Point out each leukocyte.
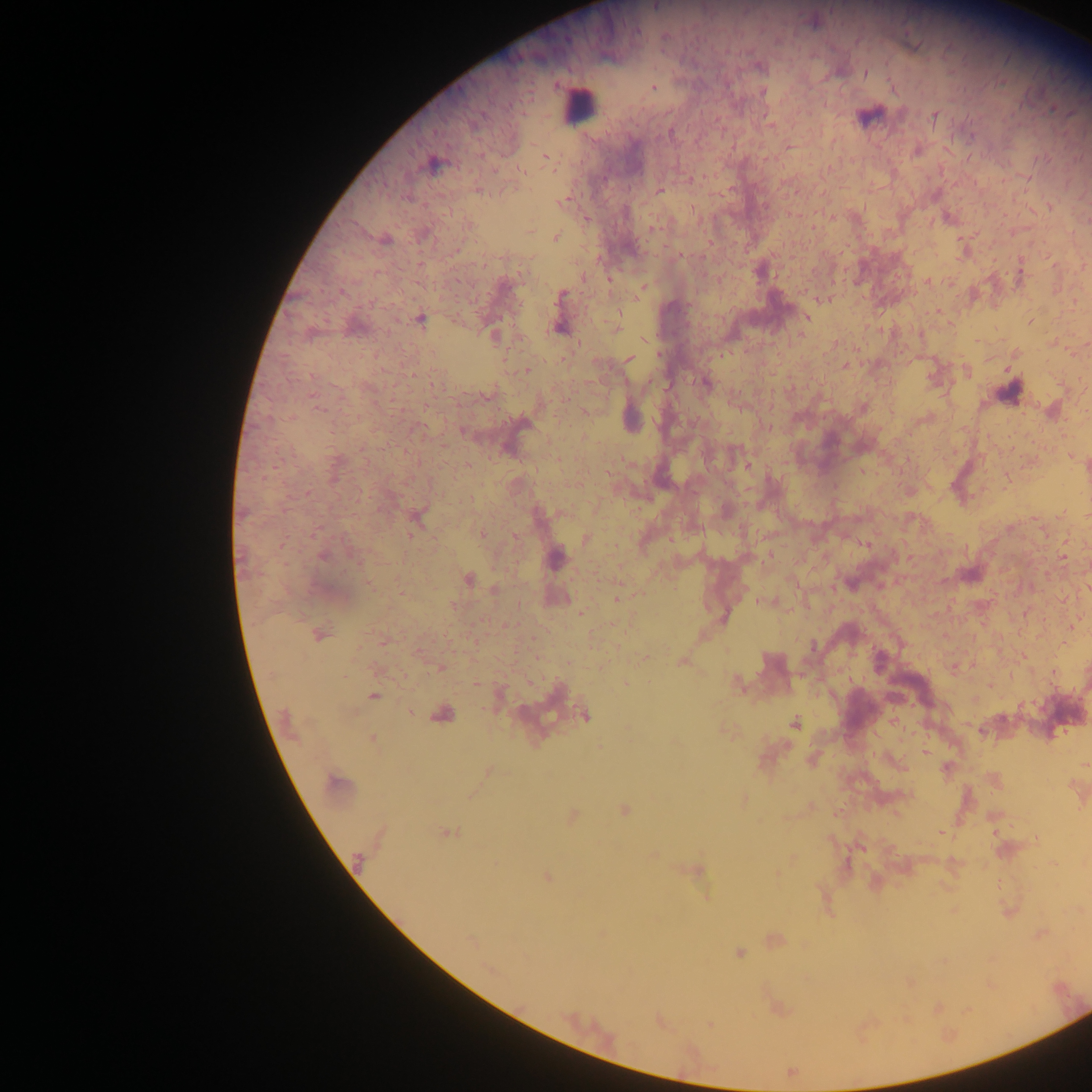

Approximate centers as x y in pixels.
Leukocytes: 578 105; 868 117; 628 420; 558 559; 969 575.

Malaria parasite locations: 655 6; 866 74; 653 88; 762 92; 934 117; 670 133; 546 157; 432 164; 521 170; 659 191; 480 192; 563 203; 468 225; 556 238; 386 240; 760 271; 583 277; 928 281; 642 287; 561 294; 824 299; 806 317; 420 320; 1031 322; 558 328; 617 328; 802 335; 494 336; 629 359; 844 366; 526 370; 966 372; 703 382; 318 409; 747 465; 481 533; 586 539; 1063 556; 322 557; 468 579; 495 590; 618 598; 581 613; 320 635; 683 662; 440 668; 475 683; 626 683; 738 684; 373 697; 411 712; 443 714; 585 716; 795 724; 373 738; 925 752; 338 784; 623 810; 572 816; 447 833; 548 876; 739 952; 711 1025. Photographed through a microscope with a mobile-phone camera. Thick blood smear. One field of view. Image is 1092×1092 pixels. Sample from Ghana.